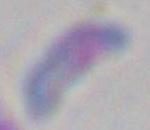

Summary:
  - Magnification: 1000x
  - Identification: Toxoplasma gondii
  - Modality: micrograph